Give a bounding box for every malaria parasite.
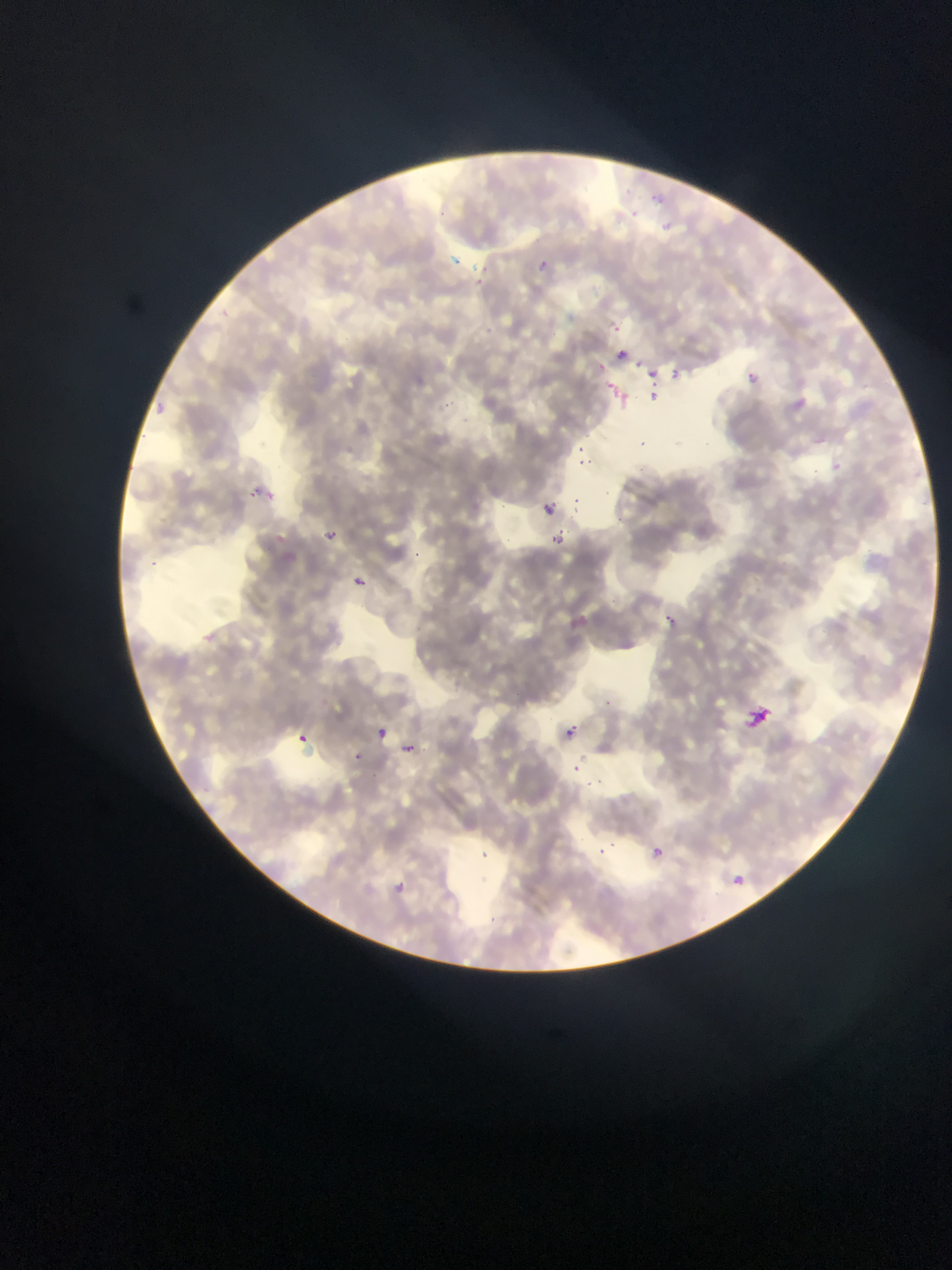
No malaria parasites observed.

Approximate bounding boxes as [left, top, right, bottom] in pixels.
Summary:
  - Artifact (stain precipitate or debris) locations: [612, 344, 665, 400], [606, 380, 633, 406], [252, 482, 269, 504], [741, 701, 767, 725]
  - Image size: 952×1270 pixels
  - Country: Ghana
  - Field of view: single
  - Capture: mobile-phone photograph through a microscope
  - Preparation: thin blood smear